Locate every Plasmodium falciparum-infected red blood cell.
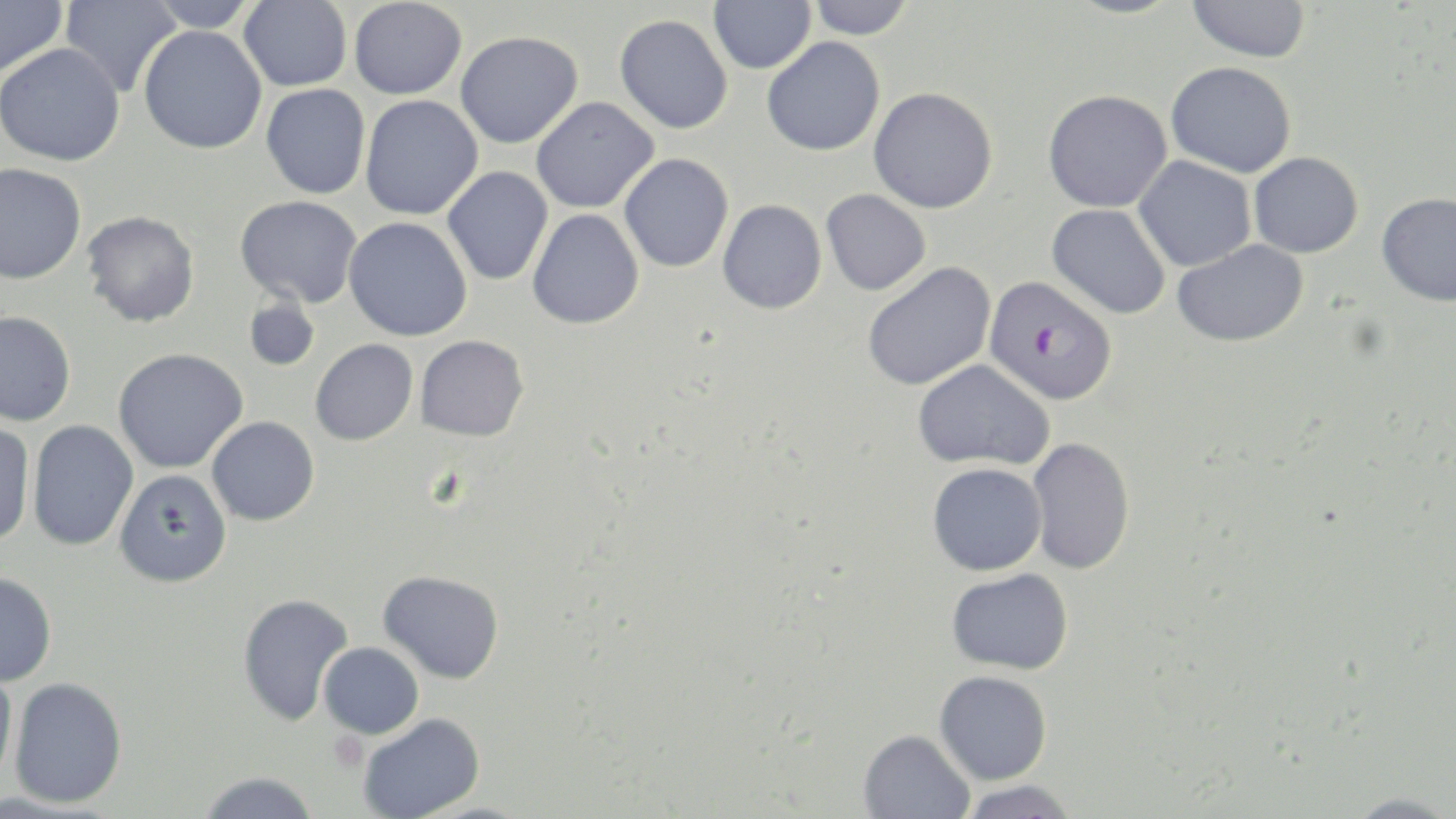

Approximate bounding boxes as (x1,y1)-(x2,y2) corner pairs in pixels.
Plasmodium falciparum-infected red blood cells: (984,275)-(1117,405).

Platelet locations: (328,731)-(367,772). Uninfected red blood cell locations: (0,0)-(68,79), (60,0)-(182,98), (143,0)-(258,32), (239,0)-(352,91), (349,0)-(466,99), (709,0)-(816,74), (1062,0)-(1186,18), (1187,0)-(1311,62), (806,1)-(915,39), (615,14)-(732,134), (138,25)-(267,154), (454,31)-(583,149), (761,36)-(885,156), (0,43)-(125,166), (1166,61)-(1296,177), (261,84)-(371,199), (869,87)-(998,213), (1043,89)-(1172,213), (360,95)-(483,220), (531,97)-(659,213), (1248,152)-(1363,258), (619,153)-(733,272), (1133,156)-(1257,272), (0,163)-(86,284), (442,166)-(553,286), (822,189)-(931,296), (1376,192)-(1456,306), (235,195)-(362,308), (717,200)-(827,314), (1046,203)-(1171,319), (527,208)-(644,329), (82,211)-(200,327), (344,216)-(472,341), (1172,240)-(1309,347), (862,261)-(996,391), (242,297)-(320,371), (0,311)-(76,426), (415,335)-(529,441), (310,339)-(418,445), (112,348)-(247,474), (913,359)-(1054,471), (207,416)-(319,525), (0,420)-(36,548), (27,420)-(138,551), (1027,437)-(1135,575), (927,463)-(1047,575), (114,469)-(232,587), (947,567)-(1074,675), (0,570)-(57,687), (378,570)-(504,684), (237,592)-(354,726), (319,641)-(424,738), (0,662)-(19,785), (934,670)-(1052,785), (8,677)-(128,808), (358,713)-(485,819), (858,729)-(975,819), (197,771)-(320,819), (958,780)-(1080,819), (1341,793)-(1456,819). Slide-level diagnosis: Plasmodium falciparum. 1000x magnification. Thin blood film. Single field of view. May-Grünwald-Giemsa stain. Image is 1456×819 pixels. Light microscopy.